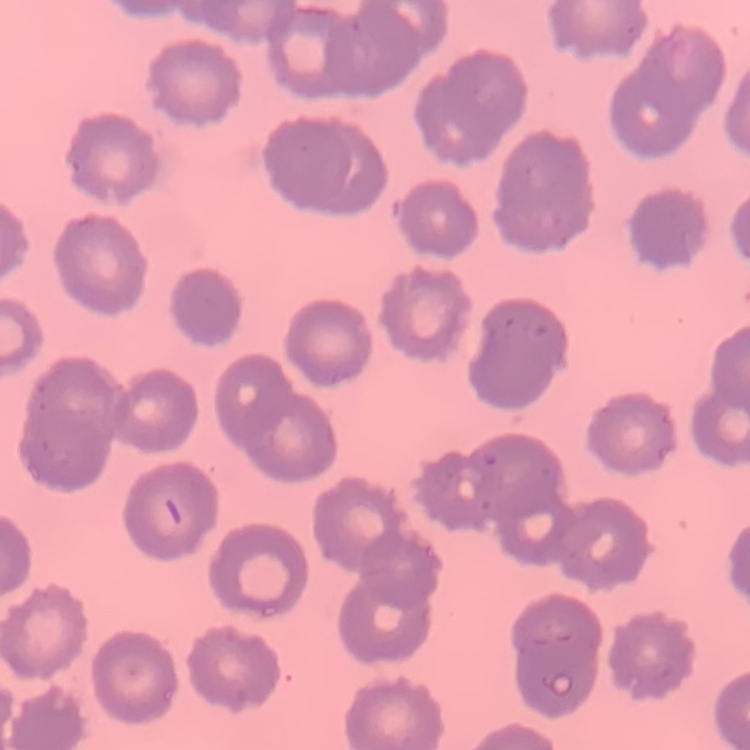
red blood cell morphology = no rouleaux formation
preparation = thin peripheral smear
stain = Field's or Giemsa
image type = square crop of a larger photomicrograph